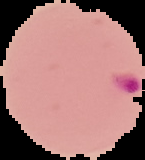

Summary:
  - Preparation: thin blood smear
  - Image type: cell region segmented out of the field of view; surrounding area masked to black
  - Result: malaria parasites detected
  - Image size: 145×160 pixels